Name the parasite shown.
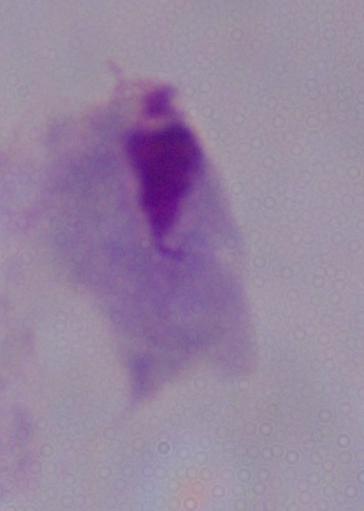
This is a trichomonad.

Summary:
  - Modality: micrograph
  - Magnification: 1000x